Assess this cell for malaria.
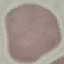
Uninfected.

Summary:
  - Image type: cell patch, automatically extracted from a larger field of view and resized to 64 × 64 pixels
  - Stain: Giemsa
  - Preparation: thin smear
  - Capture: smartphone camera at the microscope eyepiece